Assess this cell for malaria.
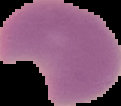

Parasitized.

Summary:
  - Preparation: thin blood film
  - Image type: segmented cell region on a black background
  - Image size: 121×106 pixels